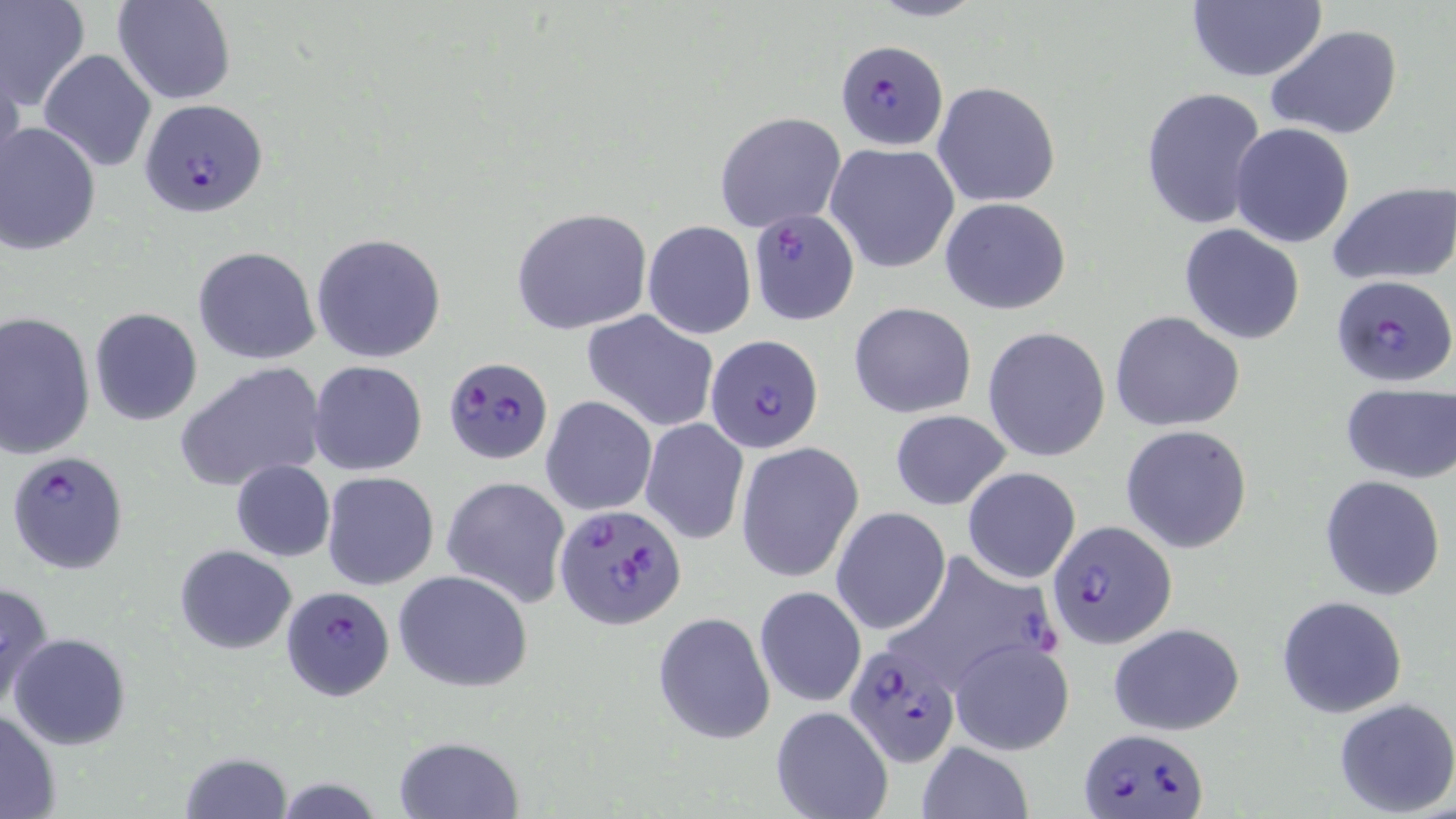

Summary:
  - Coordinate format: approximate bounding boxes as (x1,y1)-(x2,y2) corner pairs in pixels
  - Uninfected red blood cell locations: (114,0)-(235,104), (865,0)-(988,23), (0,2)-(90,112), (1185,2)-(1329,84), (1265,25)-(1404,141), (39,50)-(157,174), (0,56)-(25,193), (931,81)-(1061,207), (1141,88)-(1269,233), (715,111)-(845,233), (1,122)-(101,255), (1229,122)-(1356,248), (825,142)-(959,273), (1328,181)-(1456,286), (940,198)-(1072,314), (511,206)-(655,336), (642,221)-(756,338), (1178,224)-(1305,346), (311,233)-(445,363), (194,245)-(320,365), (849,301)-(976,418), (89,308)-(203,427), (581,309)-(720,432), (1110,310)-(1244,432), (0,311)-(96,459), (984,327)-(1110,462), (308,360)-(428,476), (175,362)-(328,493), (1340,384)-(1454,484), (540,395)-(657,515), (888,408)-(1012,511), (640,419)-(750,542), (1121,423)-(1253,554), (737,442)-(864,584), (231,459)-(335,562), (962,467)-(1081,584), (321,471)-(439,591), (442,475)-(571,608), (1320,475)-(1446,601), (832,508)-(950,636), (175,544)-(298,654), (394,569)-(533,692), (0,578)-(56,714), (755,586)-(866,708), (1276,595)-(1407,718), (652,612)-(775,745), (1106,623)-(1245,734), (10,634)-(130,750), (949,637)-(1074,756), (1333,698)-(1456,817), (770,705)-(894,819), (0,707)-(61,818), (393,736)-(521,818), (915,742)-(1032,819), (178,750)-(293,819)
  - Plasmodium falciparum-infected red blood cell locations: (835,38)-(948,149), (139,98)-(268,217), (748,208)-(860,326), (1330,273)-(1455,387), (705,334)-(825,453), (445,356)-(554,465), (6,449)-(130,577), (556,502)-(687,632), (1045,518)-(1177,648), (881,549)-(1060,697), (281,585)-(394,699), (841,642)-(960,766), (1081,726)-(1206,819)
  - Slide-level diagnosis: Plasmodium falciparum
  - Field of view: single
  - Image size: 1456×819 pixels
  - Modality: light microscopy
  - Preparation: thin blood smear
  - Magnification: 1000x
  - Stain: May-Grünwald-Giemsa